Report the malaria status of this cell.
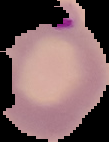

Parasitized.

Image is 109×142 pixels. From a thin blood film. Cell region segmented out of the field of view; the surrounding area is masked to black.